Give the position of every malaria parasite and every leukocyte.
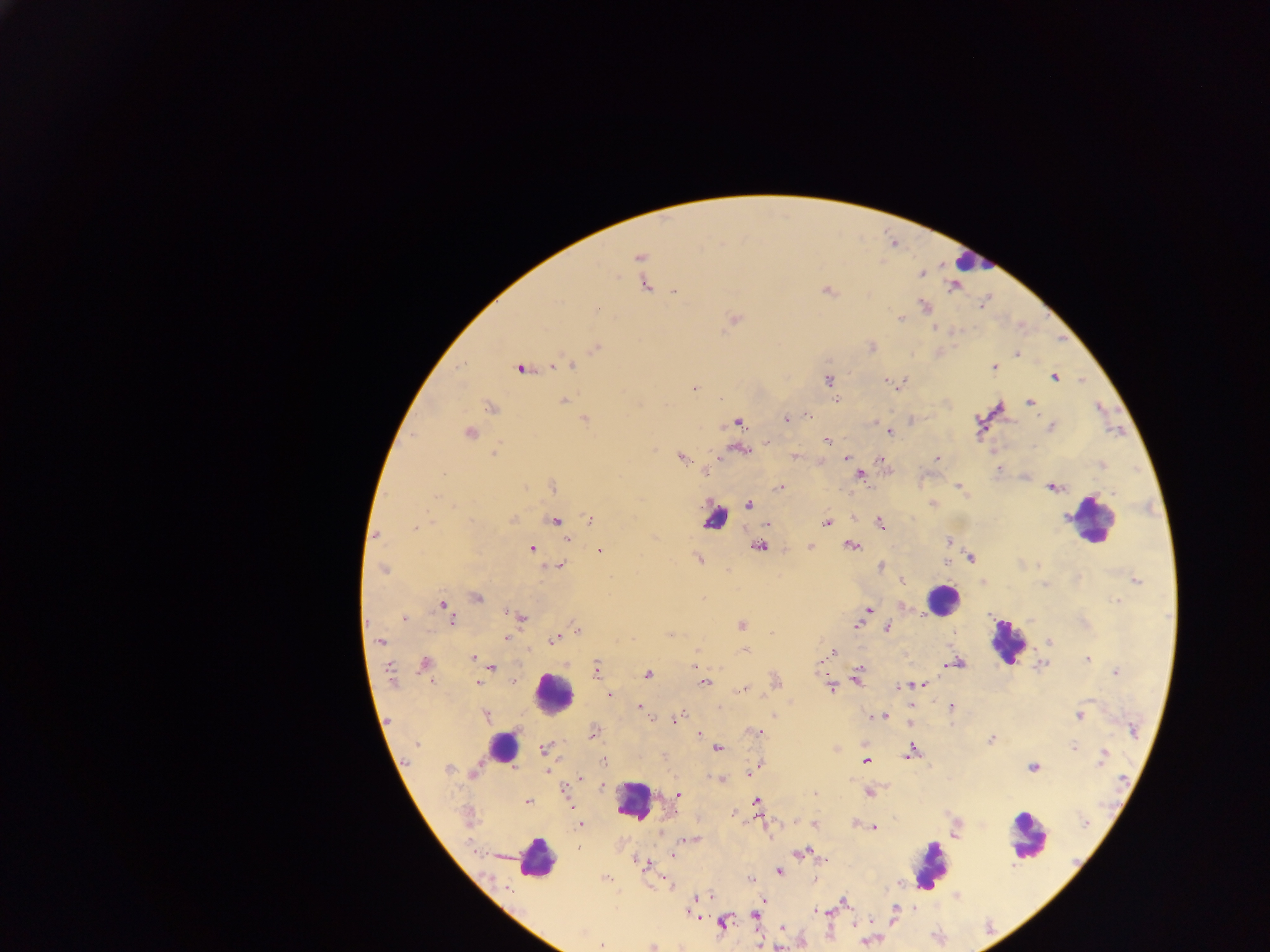

Approximate centers as {x, y} in pixels.
Malaria parasites: {638, 257}, {644, 283}, {826, 291}, {675, 292}, {596, 311}, {734, 319}, {899, 319}, {597, 347}, {1016, 354}, {1019, 354}, {572, 364}, {551, 367}, {993, 368}, {519, 369}, {1054, 376}, {884, 379}, {829, 380}, {693, 387}, {564, 401}, {1030, 401}, {491, 407}, {785, 418}, {586, 419}, {738, 422}, {470, 433}, {888, 433}, {413, 435}, {827, 440}, {767, 441}, {496, 454}, {682, 456}, {795, 457}, {844, 457}, {938, 457}, {705, 471}, {860, 474}, {956, 485}, {779, 487}, {1050, 488}, {961, 489}, {748, 503}, {932, 504}, {1066, 517}, {513, 519}, {591, 519}, {555, 520}, {826, 522}, {416, 527}, {376, 535}, {566, 539}, {947, 541}, {760, 546}, {810, 546}, {851, 546}, {531, 549}, {599, 550}, {971, 557}, {700, 559}, {946, 563}, {561, 566}, {881, 566}, {383, 569}, {901, 581}, {1136, 581}, {982, 585}, {478, 597}, {1116, 601}, {442, 604}, {869, 608}, {505, 613}, {404, 617}, {521, 617}, {453, 619}, {405, 620}, {740, 624}, {858, 626}, {888, 628}, {670, 634}, {506, 638}, {553, 638}, {1051, 641}, {382, 642}, {528, 649}, {744, 649}, {834, 651}, {474, 658}, {1086, 659}, {820, 662}, {956, 662}, {424, 663}, {945, 665}, {596, 666}, {389, 668}, {494, 669}, {696, 669}, {1115, 672}, {648, 674}, {857, 677}, {435, 679}, {513, 680}, {391, 681}, {479, 682}, {705, 683}, {903, 685}, {831, 687}, {739, 690}, {610, 693}, {639, 706}, {950, 706}, {684, 714}, {485, 715}, {646, 715}, {869, 716}, {882, 716}, {1080, 717}, {678, 718}, {755, 732}, {699, 733}, {991, 738}, {417, 743}, {911, 746}, {1073, 747}, {835, 748}, {543, 750}, {718, 750}, {1103, 750}, {907, 753}, {866, 760}, {604, 762}, {1101, 763}, {1033, 767}, {449, 769}, {474, 772}, {748, 772}, {719, 778}, {580, 779}, {601, 785}, {813, 792}, {869, 792}, {678, 795}, {756, 800}, {528, 801}, {735, 811}, {791, 821}, {854, 823}, {580, 824}, {763, 824}, {814, 824}, {876, 827}, {671, 853}, {797, 853}, {642, 860}, {780, 871}, {604, 877}, {710, 895}, {844, 900}, {693, 901}, {815, 909}, {754, 916}, {722, 922}, {600, 944}, {652, 947}.
Leukocytes: {972, 261}, {716, 521}, {1093, 525}, {939, 598}, {1006, 642}, {550, 695}, {505, 746}, {633, 803}, {1030, 835}, {535, 858}, {932, 865}.

field of view = single
capture = mobile-phone photograph through a microscope
preparation = thick blood smear
country = Ghana
image size = 1270×952 pixels